Assess the morphology of the red blood cells.
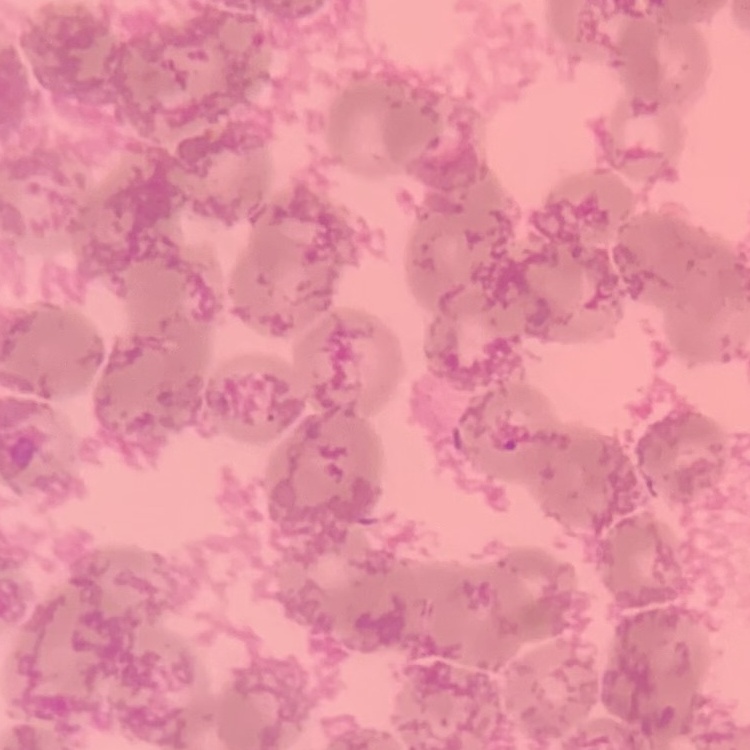

Rouleaux formation.

Summary:
  - Preparation: thin blood smear
  - Image type: one tile cut from a larger photomicrograph
  - Stain: Field's or Giemsa